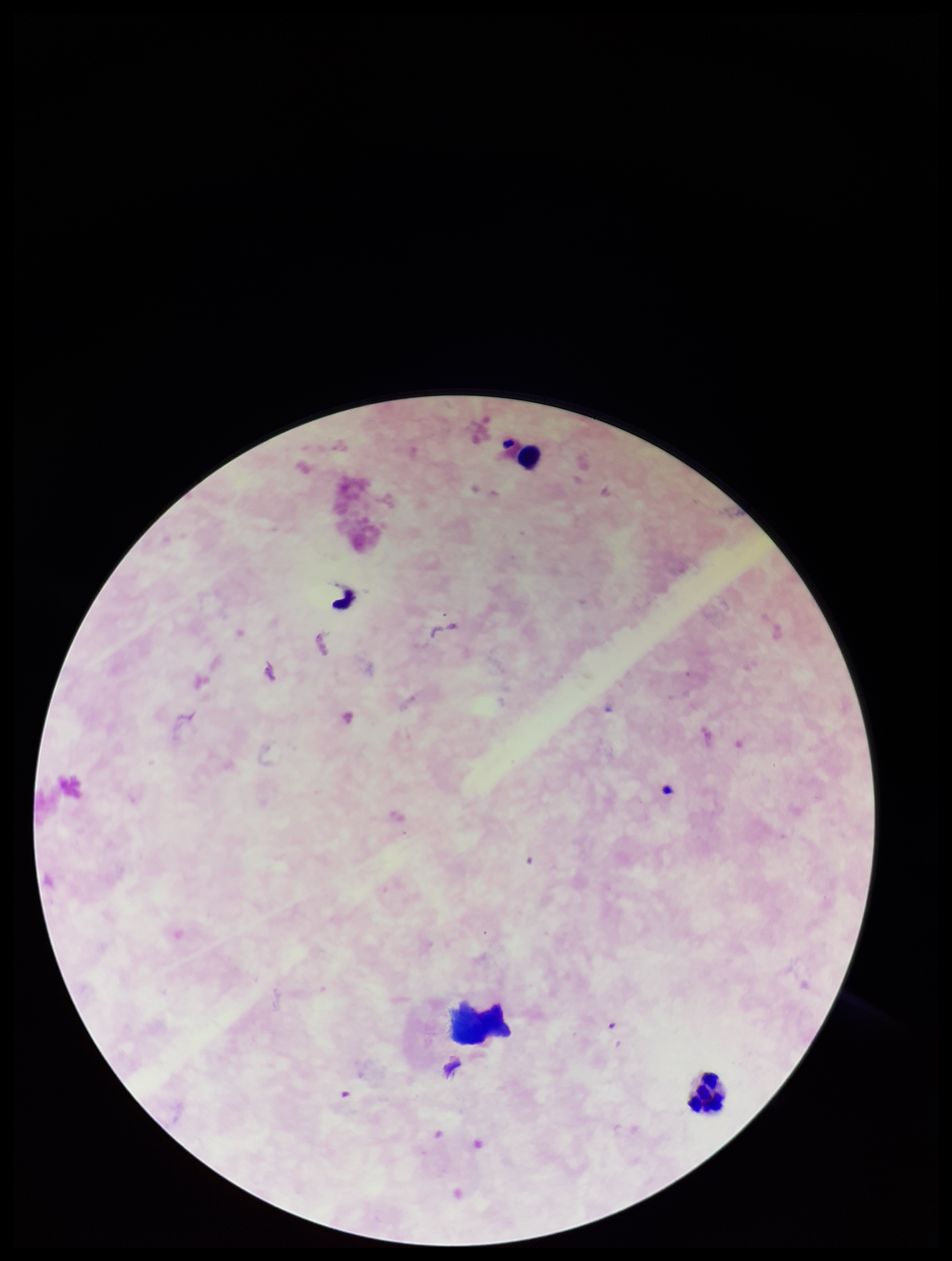
leukocyte count = 2
Plasmodium parasites = none seen
preparation = thick smear
field of view = one from this slide
capture = smartphone photograph through the microscope eyepiece
image size = 952×1261 pixels
parasite count = 0
patient malaria status = negative
stain = Giemsa